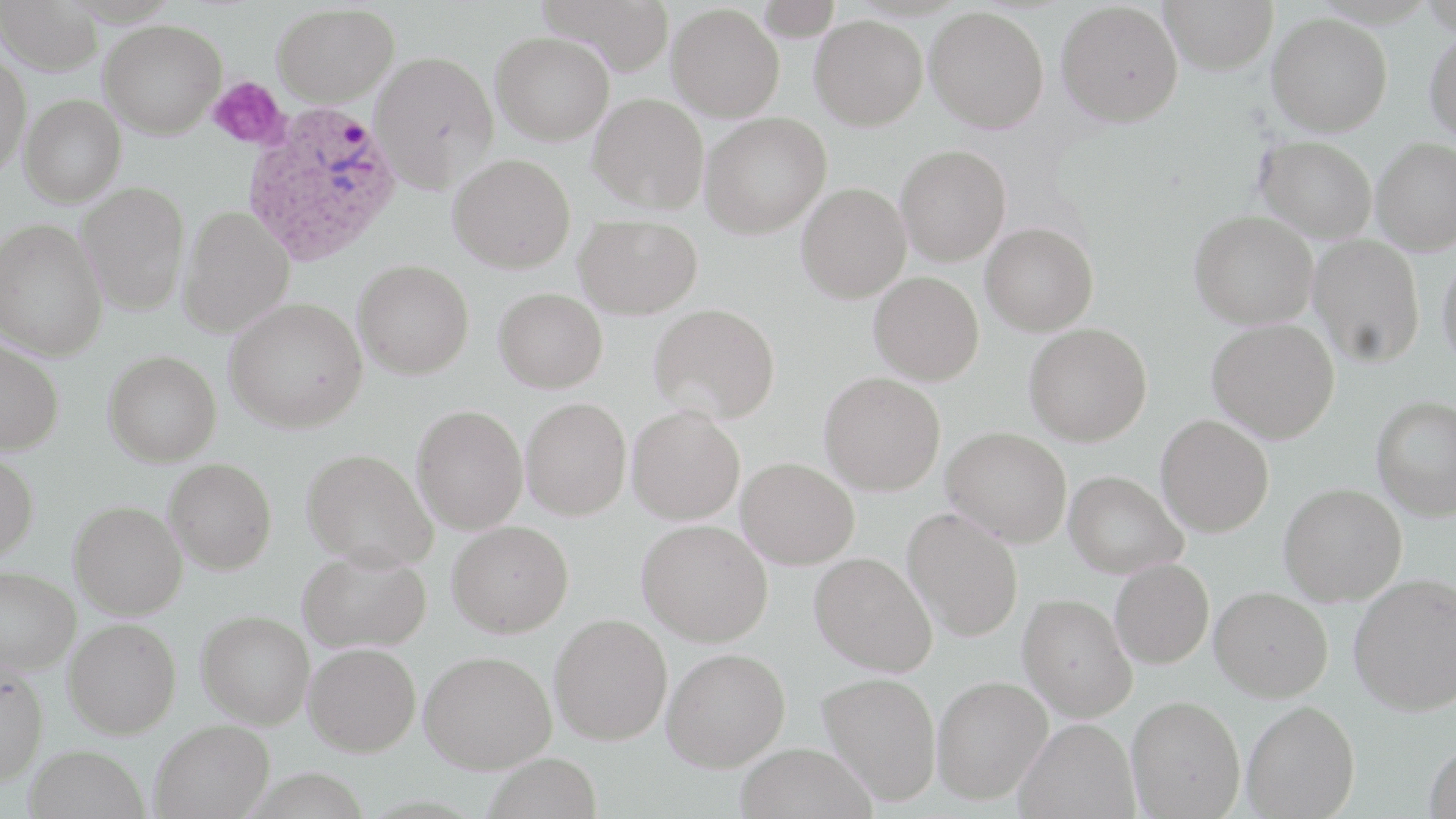 Approximate bounding boxes as (x1, y1, x2, y2) in pixels. Platelet locations: (208, 77, 288, 150). Uninfected red blood cell locations: (0, 0, 102, 75), (537, 0, 676, 75), (1159, 0, 1278, 74), (1056, 2, 1183, 127), (271, 3, 398, 107), (667, 4, 784, 122), (925, 7, 1049, 133), (1267, 13, 1392, 135), (810, 16, 927, 130), (99, 20, 227, 139), (1424, 30, 1456, 145), (491, 31, 614, 144), (0, 49, 31, 176), (371, 51, 499, 193), (589, 93, 709, 214), (20, 94, 126, 206), (700, 112, 831, 238), (1255, 135, 1376, 243), (1372, 138, 1456, 255), (895, 144, 1011, 265), (448, 153, 575, 273), (76, 181, 191, 315), (796, 182, 911, 303), (178, 204, 295, 338), (1189, 211, 1318, 329), (574, 215, 703, 319), (0, 218, 107, 361), (981, 222, 1098, 335), (1308, 235, 1424, 367), (1437, 251, 1456, 372), (353, 259, 474, 379), (869, 271, 984, 384), (493, 288, 607, 393), (224, 296, 368, 433), (649, 303, 780, 424), (1207, 319, 1339, 443), (1024, 323, 1152, 446), (0, 337, 64, 455), (103, 350, 221, 466), (819, 372, 945, 495), (1371, 396, 1456, 521), (521, 397, 632, 520), (411, 404, 528, 534), (627, 406, 745, 524), (1156, 415, 1274, 536), (942, 427, 1072, 547), (300, 448, 437, 570), (0, 450, 38, 563), (163, 458, 277, 574), (736, 458, 859, 569), (1064, 470, 1187, 579), (1278, 482, 1406, 606), (69, 501, 187, 619), (902, 507, 1023, 642), (637, 518, 773, 646), (447, 520, 573, 638), (297, 546, 431, 653), (809, 552, 937, 676), (1110, 558, 1214, 669), (0, 565, 80, 674), (1348, 573, 1456, 715), (1210, 586, 1333, 701), (1018, 593, 1136, 721), (196, 610, 314, 728), (549, 613, 672, 745), (64, 617, 181, 738), (303, 642, 421, 756), (662, 647, 790, 771), (419, 650, 556, 773), (0, 663, 49, 785), (818, 671, 941, 805), (932, 675, 1053, 804), (1126, 695, 1245, 818), (1241, 700, 1360, 818), (1015, 717, 1139, 819), (150, 719, 274, 818), (1424, 740, 1456, 819), (734, 742, 877, 819), (23, 744, 149, 819), (483, 752, 603, 819). Plasmodium ovale-infected red blood cell locations: (243, 99, 402, 266). Slide-level diagnosis: Plasmodium ovale. May-Grünwald-Giemsa stain. 1000x magnification. Single field of view. Image is 1456×819 pixels. Optical microscopy. Thin blood film.